Identify the cell.
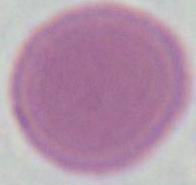
This is an erythrocyte.

Summary:
  - Modality: micrograph
  - Magnification: 1000x